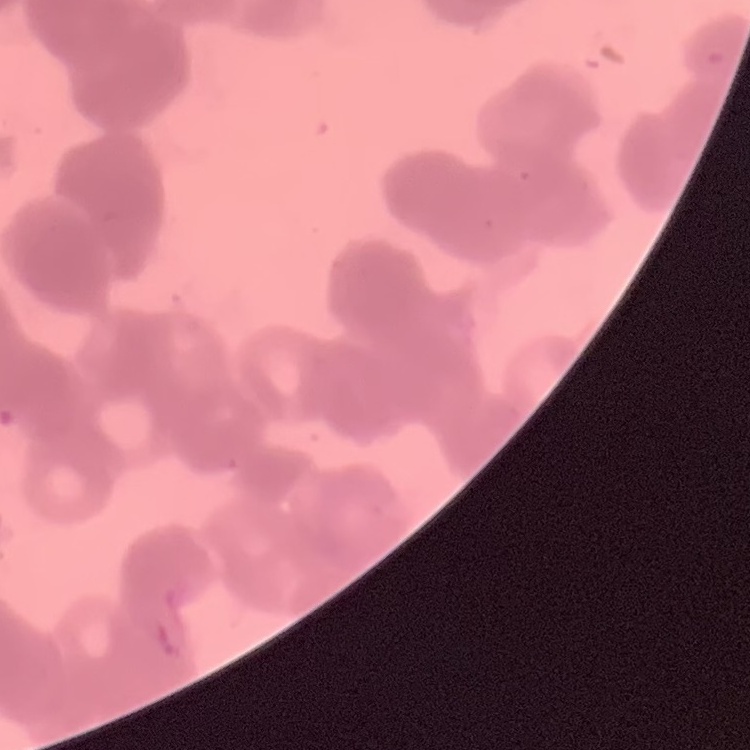

The erythrocytes show rouleaux formation. Square crop of a larger photomicrograph. Field's or Giemsa stain. Thin blood film.